Assess this cell for malaria.
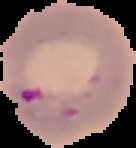
It is parasitized.

Image is 136×148 pixels. Segmented cell region on a black background. From a thin blood smear.